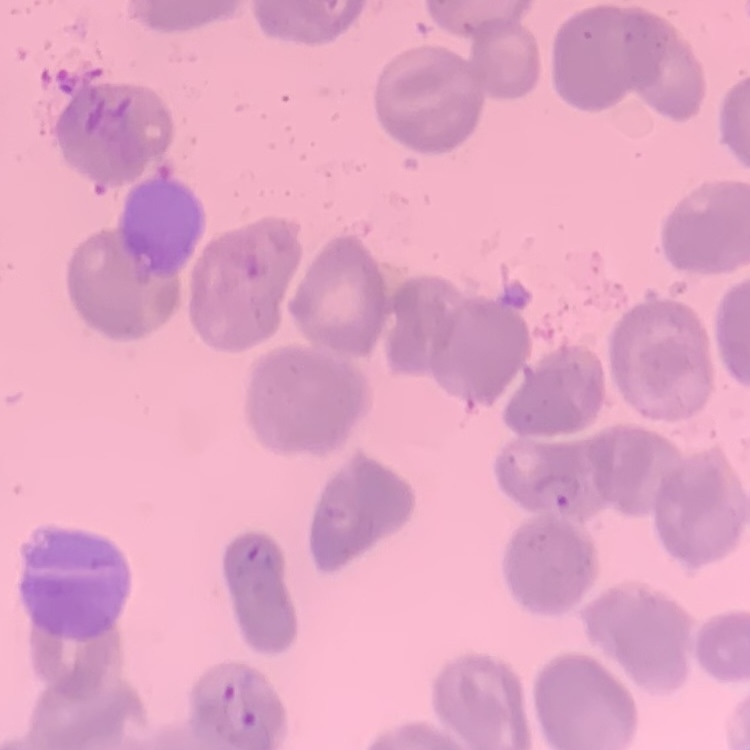 The erythrocytes show no rouleaux formation. Thin blood film. One tile cut from a larger photomicrograph. Stained with either Field's or Giemsa.